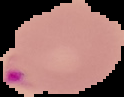
Summary:
  - Image size: 124×97 pixels
  - Malaria status: parasitized
  - Preparation: thin blood film
  - Image type: segmented cell region with the area outside set to black